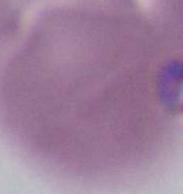 An erythrocyte is seen. 1000x magnification. Photomicrograph.